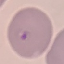
Summary:
  - Malaria status: parasitized
  - Stain: Giemsa
  - Capture: smartphone through the microscope eyepiece
  - Preparation: thin blood film
  - Image type: automatically extracted cell patch, resized to 64 × 64 pixels